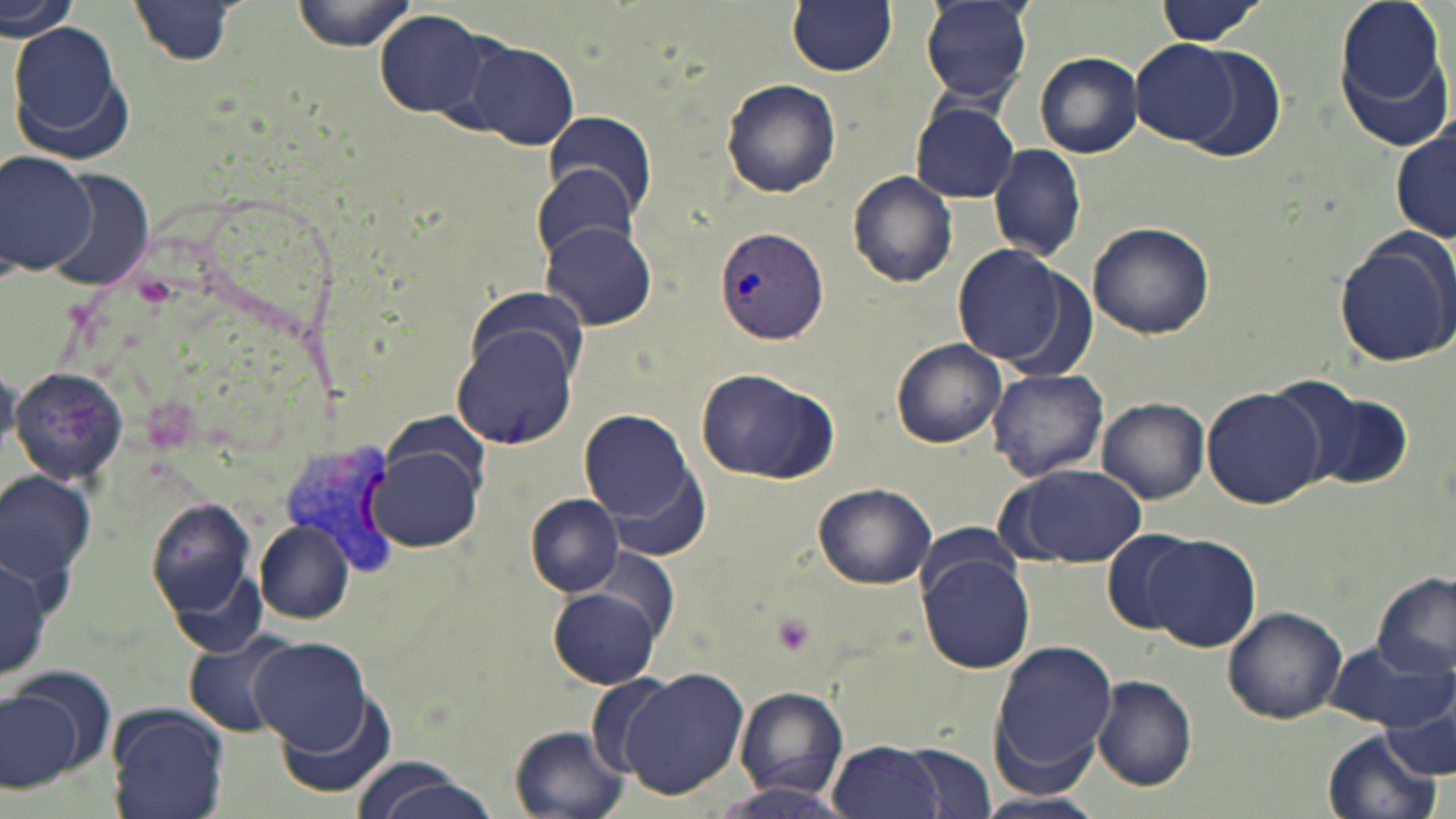
Summary:
  - Coordinate format: approximate bounding boxes as [x1, y1, x2, y2] in pixels
  - Uninfected red blood cell locations: [0, 0, 82, 40], [293, 0, 416, 51], [787, 0, 897, 75], [1152, 0, 1267, 47], [1331, 0, 1455, 153], [919, 1, 1033, 107], [129, 2, 238, 66], [373, 8, 495, 121], [8, 22, 132, 159], [462, 39, 580, 150], [1131, 39, 1243, 145], [1177, 46, 1285, 163], [1035, 52, 1142, 159], [721, 77, 841, 198], [909, 101, 1020, 204], [542, 111, 655, 216], [1391, 125, 1456, 244], [988, 142, 1087, 261], [0, 149, 97, 278], [533, 166, 641, 263], [48, 170, 152, 294], [848, 170, 957, 286], [541, 220, 659, 332], [1087, 220, 1216, 339], [1331, 229, 1455, 367], [951, 242, 1078, 370], [451, 321, 580, 449], [891, 339, 1007, 449], [11, 366, 130, 485], [695, 367, 840, 486], [988, 368, 1109, 481], [1267, 376, 1405, 492], [1204, 387, 1326, 510], [1098, 396, 1209, 503], [577, 408, 700, 530], [369, 444, 486, 551], [608, 463, 714, 563], [997, 464, 1148, 569], [1, 473, 95, 588], [812, 481, 937, 590], [526, 494, 624, 595], [147, 497, 262, 638], [253, 519, 354, 624], [1101, 528, 1210, 633], [1138, 533, 1260, 651], [917, 552, 1034, 674], [0, 558, 53, 680], [1372, 572, 1454, 683], [548, 579, 666, 691], [1223, 607, 1347, 724], [181, 631, 299, 738], [249, 637, 374, 752], [987, 640, 1116, 786], [1325, 642, 1452, 732], [11, 663, 116, 772], [618, 667, 750, 799], [584, 673, 675, 777], [1091, 675, 1198, 791], [0, 686, 80, 790], [734, 687, 847, 798], [276, 690, 397, 800], [107, 706, 228, 819], [1379, 713, 1455, 779], [510, 726, 629, 818], [1323, 730, 1441, 819], [827, 738, 947, 819], [890, 739, 1000, 816], [349, 758, 505, 819], [709, 784, 860, 819], [970, 791, 1106, 819]
  - Plasmodium vivax-infected red blood cell locations: [713, 225, 829, 347], [277, 437, 399, 574]
  - Platelet locations: [768, 613, 816, 656]
  - Slide-level diagnosis: Plasmodium vivax
  - Stain: May-Grünwald-Giemsa
  - Field of view: one of a larger specimen
  - Image size: 1456×819 pixels
  - Modality: light microscopy
  - Magnification: 1000x
  - Preparation: thin blood film